Assess this cell for malaria.
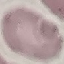

It is uninfected.

Summary:
  - Stain: Giemsa
  - Preparation: thin blood smear
  - Capture: smartphone camera at the microscope eyepiece
  - Image type: automatically extracted cell patch, resized to 64 × 64 pixels